Point out each Plasmodium parasite.
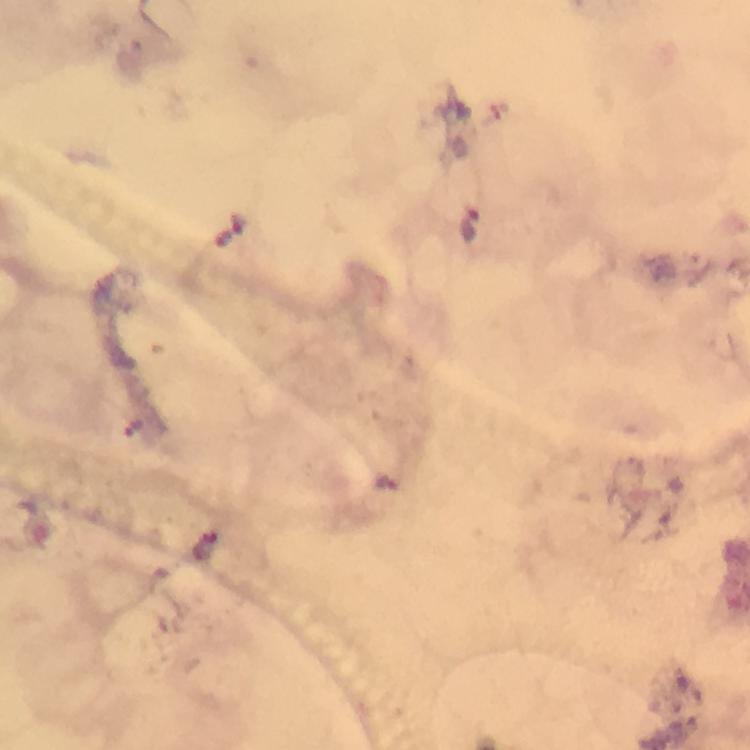

Approximate object centers, in pixels from the top-left corner.
Plasmodium parasites: (x=467, y=228), (x=228, y=236), (x=133, y=428), (x=388, y=483), (x=205, y=548).

preparation = thick blood film
cropped from = one field of view
capture = smartphone photograph through a microscope
image size = 750×750 pixels
stain = Giemsa
magnification = 100x
context = from a diagnostic examination for malaria
immersion oil = used